Locate leukocytes (white blood cells).
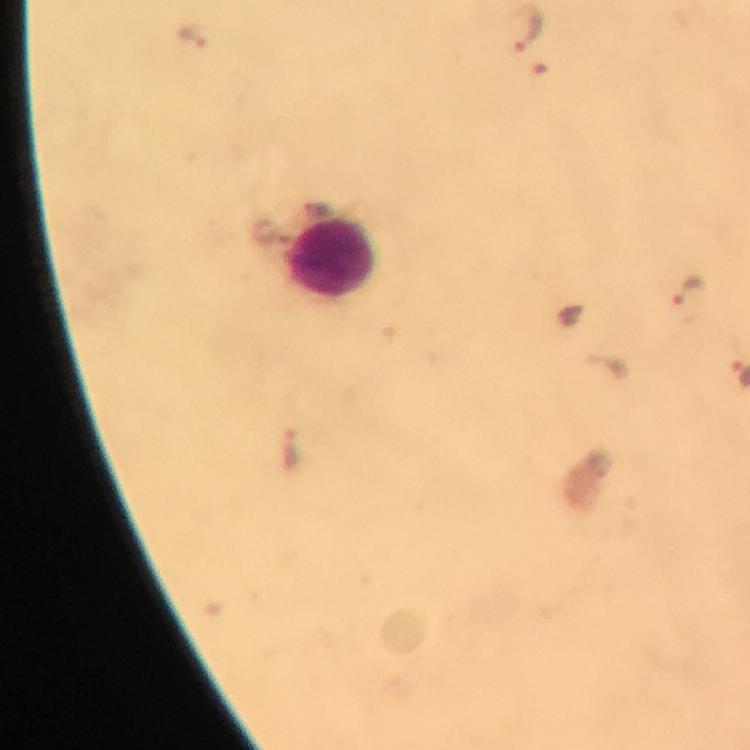
Approximate centers as [x, y] in pixels.
Leukocytes: [334, 258].

context = from a diagnostic examination for malaria
stain = Giemsa
image size = 750×750 pixels
malaria parasite locations = approximate centers as [x, y] in pixels: [526, 28], [192, 36], [690, 290], [293, 447]
immersion oil = used
preparation = thick smear
magnification = 100x
capture = smartphone camera through the microscope
cropped from = one field of view